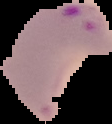
{
  "image_type": "segmented cell region with the area outside set to black",
  "preparation": "thin blood smear",
  "result": "Plasmodium parasites detected",
  "image_size": "112×124 pixels"
}